Assess this cell for malaria.
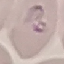
It is parasitized.

stain = Giemsa
capture = smartphone through the microscope eyepiece
preparation = thin blood film
image type = cell patch, automatically extracted from a larger field of view and resized to 64 × 64 pixels